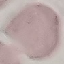
result = negative for malaria parasites
preparation = thin blood film
image type = cell patch, automatically extracted from a larger field of view and resized to 64 × 64 pixels
capture = smartphone camera at the microscope eyepiece
stain = Giemsa